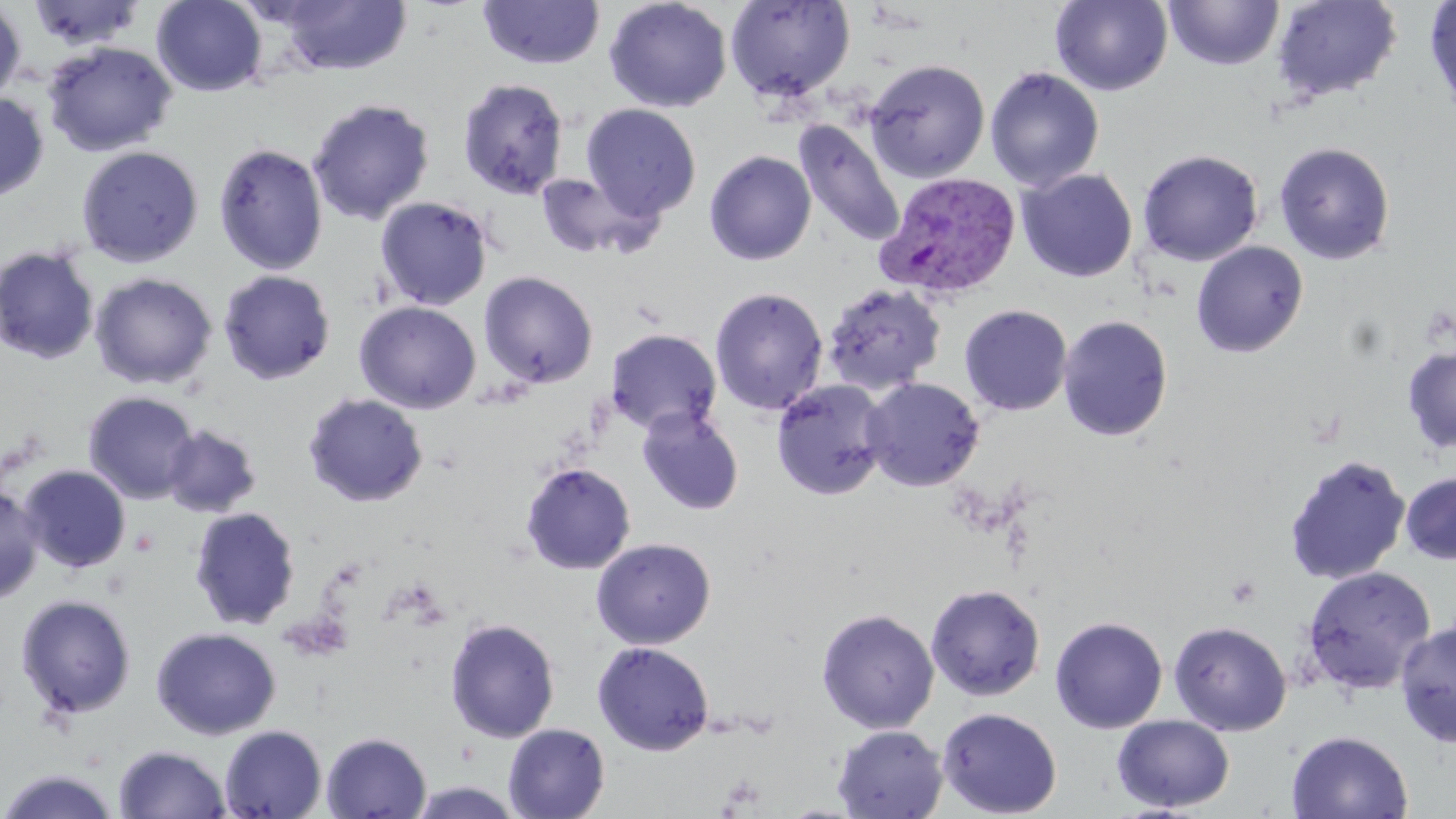 Approximate bounding boxes as [x1, y1, x2, y2] in pixels. Plasmodium vivax-infected red blood cell locations: [875, 171, 1022, 302]. Uninfected red blood cell locations: [151, 0, 268, 96], [268, 0, 413, 77], [476, 0, 605, 70], [604, 0, 732, 113], [1050, 0, 1173, 96], [1271, 0, 1402, 105], [1424, 0, 1456, 122], [27, 1, 146, 52], [725, 1, 855, 100], [1164, 1, 1284, 71], [0, 2, 26, 106], [41, 41, 178, 157], [60, 43, 187, 266], [864, 59, 990, 183], [985, 67, 1105, 193], [457, 77, 570, 200], [0, 92, 50, 203], [307, 97, 435, 226], [581, 104, 701, 221], [793, 120, 905, 250], [1273, 141, 1396, 265], [213, 142, 329, 276], [76, 145, 204, 268], [1137, 149, 1264, 266], [704, 150, 816, 265], [1017, 168, 1138, 282], [532, 171, 661, 261], [375, 196, 493, 311], [1191, 241, 1309, 358], [0, 245, 100, 366], [218, 270, 336, 385], [479, 271, 598, 389], [89, 272, 217, 390], [821, 283, 947, 396], [710, 287, 828, 416], [354, 301, 481, 414], [959, 304, 1072, 416], [1058, 315, 1173, 442], [606, 328, 722, 435], [1402, 347, 1456, 453], [861, 377, 984, 491], [771, 379, 891, 501], [82, 391, 200, 504], [303, 392, 429, 507], [637, 407, 745, 516], [162, 424, 262, 518], [1283, 453, 1411, 586], [520, 462, 636, 575], [19, 464, 131, 573], [1400, 471, 1456, 565], [0, 483, 44, 606], [188, 507, 301, 630], [591, 538, 716, 649], [1301, 566, 1436, 695], [925, 583, 1046, 701], [15, 593, 137, 720], [816, 608, 940, 733], [1049, 616, 1168, 733], [444, 617, 560, 742], [1168, 621, 1292, 736], [1395, 621, 1456, 749], [151, 627, 281, 740], [592, 641, 714, 755], [937, 707, 1062, 818], [1112, 714, 1235, 812], [503, 722, 610, 819], [219, 724, 328, 819], [832, 725, 947, 819], [1287, 730, 1413, 819], [321, 732, 431, 818], [113, 745, 231, 818], [0, 768, 124, 819]. Slide-level diagnosis: Plasmodium vivax. One field of a larger specimen. Captured at 1000x magnification. Thin blood smear. May-Grünwald-Giemsa-stained preparation. Optical microscopy. Image is 1456×819 pixels.